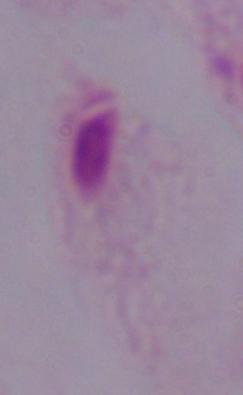
Summary:
  - Modality: photomicrograph
  - Identification: trichomonad
  - Magnification: 1000x